Give the position of every leukocyte visible.
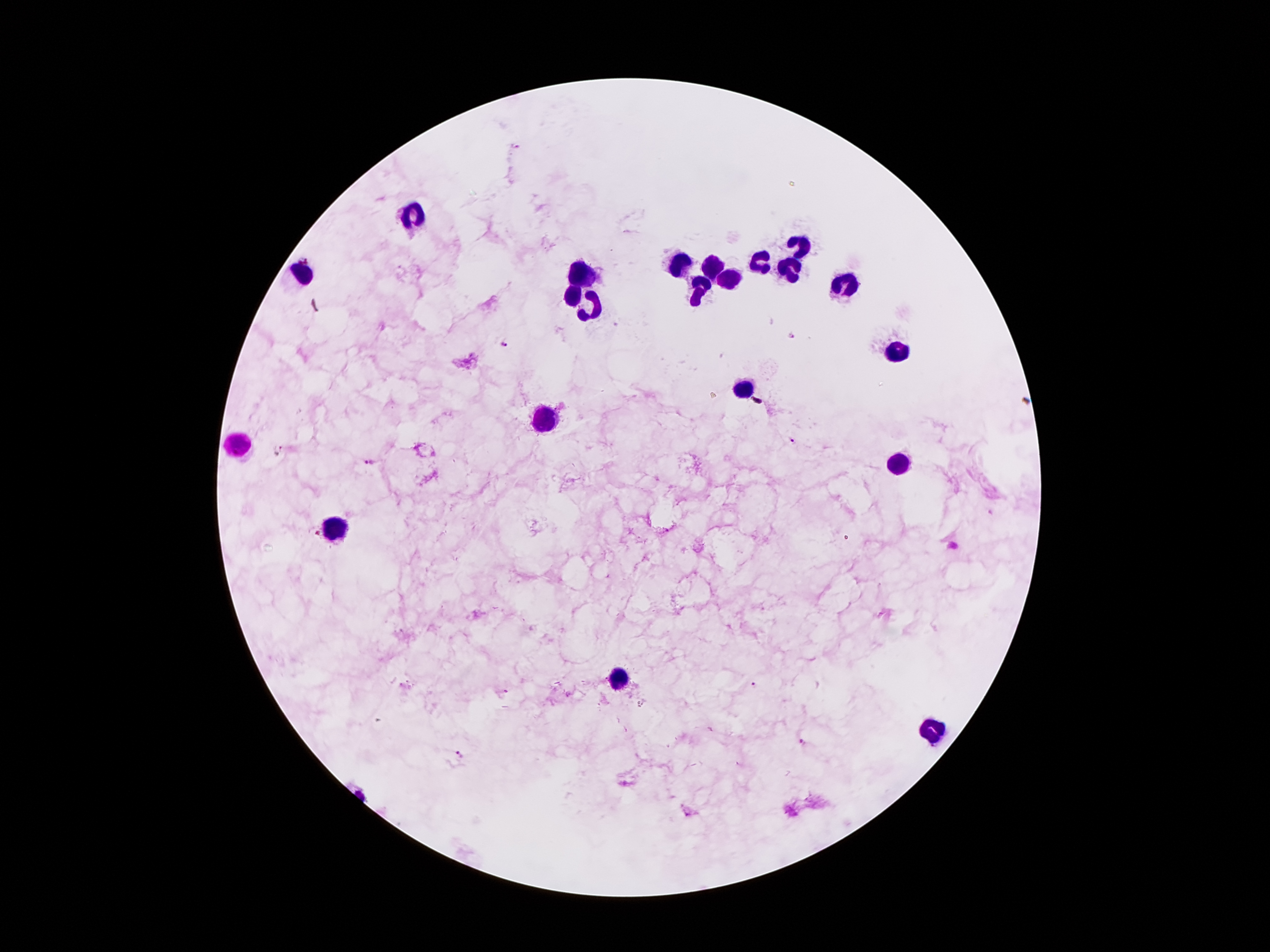

Approximate object centers, in pixels from the top-left corner.
Leukocytes: (x=412, y=217), (x=802, y=246), (x=682, y=260), (x=762, y=260), (x=714, y=263), (x=304, y=271), (x=582, y=271), (x=790, y=273), (x=727, y=281), (x=842, y=282), (x=699, y=290), (x=569, y=292), (x=594, y=309), (x=899, y=353), (x=743, y=388), (x=546, y=422), (x=237, y=444), (x=897, y=464), (x=334, y=527), (x=619, y=676), (x=934, y=725).

capture: smartphone camera through the microscope eyepiece
preparation: thick blood film
image_size: 1270×952 pixels
field_of_view: one from this slide
magnification: 100x
plasmodium_parasite_locations: 'approximate object centers, in pixels from the top-left corner: (x=794, y=335), (x=501, y=342), (x=794, y=440), (x=283, y=448), (x=371, y=463), (x=753, y=685), (x=801, y=742), (x=460, y=754)'
patient_malaria_status: infected with Plasmodium falciparum
stain: Giemsa